Give a bounding box for every leukocyte visible.
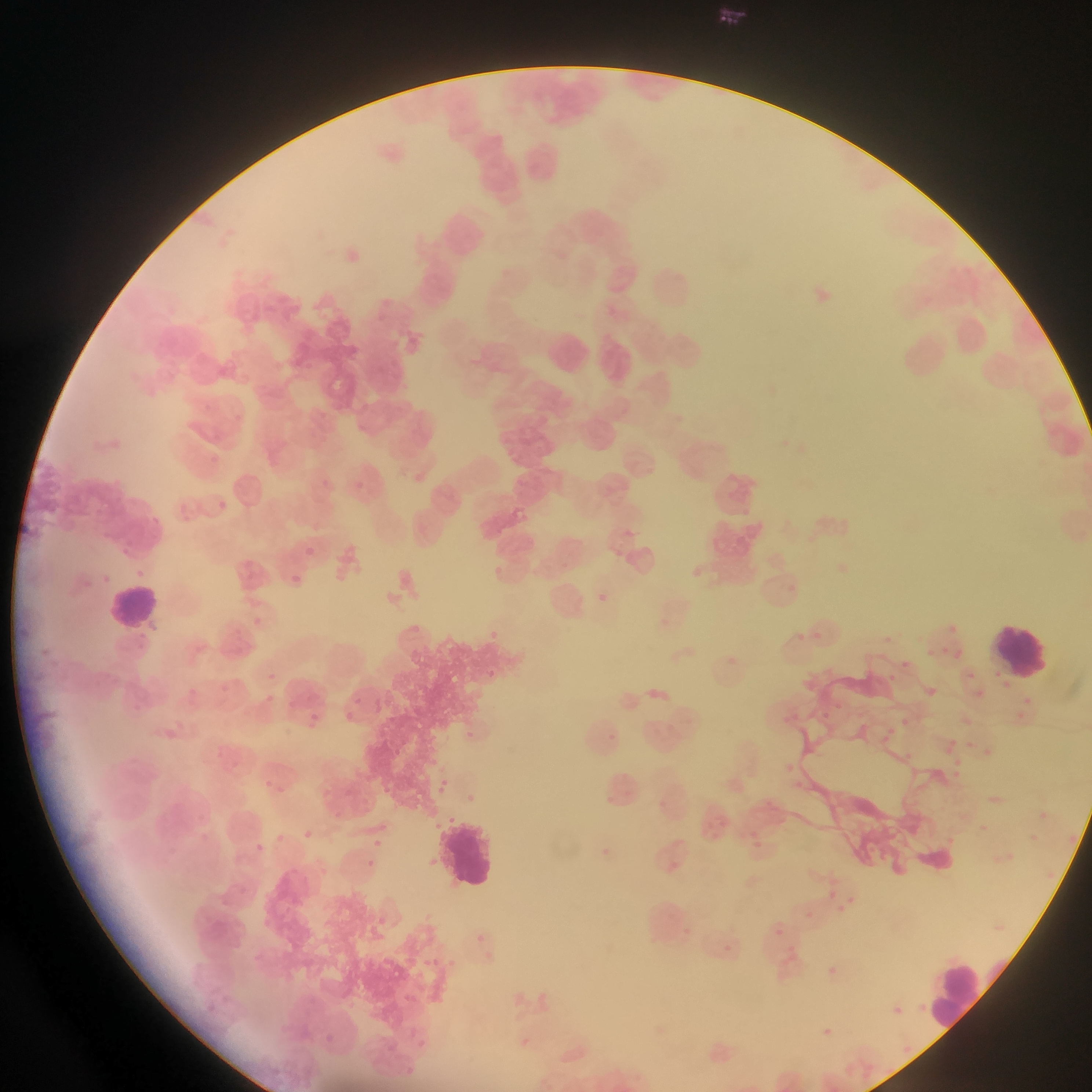
Approximate bounding boxes as (left, top, right, bottom) in pixels.
Leukocytes: (107, 583, 162, 635), (995, 619, 1054, 677), (441, 817, 499, 887), (931, 961, 991, 1036).

Plasmodium parasite locations: (209, 450, 226, 468), (321, 479, 331, 489), (355, 481, 364, 490), (178, 500, 193, 517), (218, 501, 227, 510), (145, 511, 164, 529), (113, 542, 135, 558), (304, 546, 315, 556), (492, 566, 499, 575), (135, 567, 147, 577), (98, 570, 110, 584), (290, 571, 313, 590), (788, 583, 795, 592), (596, 593, 617, 613), (949, 624, 957, 632), (490, 626, 513, 647), (797, 629, 803, 639), (810, 629, 828, 639), (883, 635, 891, 642), (940, 641, 952, 655), (922, 645, 932, 663), (949, 647, 967, 663), (902, 657, 911, 669), (266, 664, 288, 688), (482, 667, 498, 676), (885, 672, 897, 683), (997, 676, 1017, 689), (220, 679, 233, 697), (188, 685, 205, 703), (925, 685, 940, 701), (1023, 691, 1032, 704), (127, 695, 147, 723), (264, 697, 284, 711), (374, 697, 391, 717), (829, 701, 839, 707), (341, 705, 359, 731), (1011, 706, 1023, 727), (817, 709, 829, 723), (310, 711, 326, 724), (898, 712, 913, 730), (164, 724, 183, 741), (880, 724, 893, 746), (602, 728, 621, 748), (466, 730, 480, 743), (945, 733, 958, 748), (965, 740, 974, 748), (979, 741, 997, 757), (391, 745, 405, 757), (901, 747, 913, 760), (952, 756, 966, 768), (784, 762, 796, 778), (953, 769, 962, 785), (440, 774, 456, 789), (437, 784, 446, 796), (279, 785, 291, 799), (465, 791, 477, 805), (603, 792, 621, 808), (1037, 808, 1048, 820), (428, 818, 438, 827), (979, 821, 995, 835), (1068, 827, 1081, 844), (306, 828, 320, 841), (744, 828, 766, 855), (1027, 829, 1039, 840), (274, 832, 286, 841), (943, 832, 955, 847), (374, 836, 390, 852), (249, 839, 269, 855), (601, 844, 615, 859), (432, 854, 443, 866), (668, 857, 682, 871), (368, 860, 381, 870), (824, 883, 836, 899), (849, 893, 862, 912), (801, 904, 811, 911), (839, 905, 845, 921), (371, 913, 383, 927), (774, 927, 784, 937), (472, 930, 488, 948), (725, 940, 734, 956), (421, 951, 443, 974), (448, 953, 462, 969), (825, 963, 841, 979), (402, 985, 417, 1001), (916, 998, 933, 1018), (204, 999, 220, 1019), (893, 1005, 900, 1019), (819, 1022, 835, 1042), (323, 1028, 336, 1045), (420, 1028, 432, 1050), (515, 1034, 535, 1052), (388, 1038, 403, 1052), (903, 1046, 911, 1052), (398, 1060, 412, 1081) | approximate (x, y) pixel centers of objects too small to bound: (268, 781). Mobile-phone photograph taken through the microscope. Thin blood film. Image is 1092×1092 pixels. Sample from Ghana. Single field of view.